Assess the morphology of the erythrocytes.
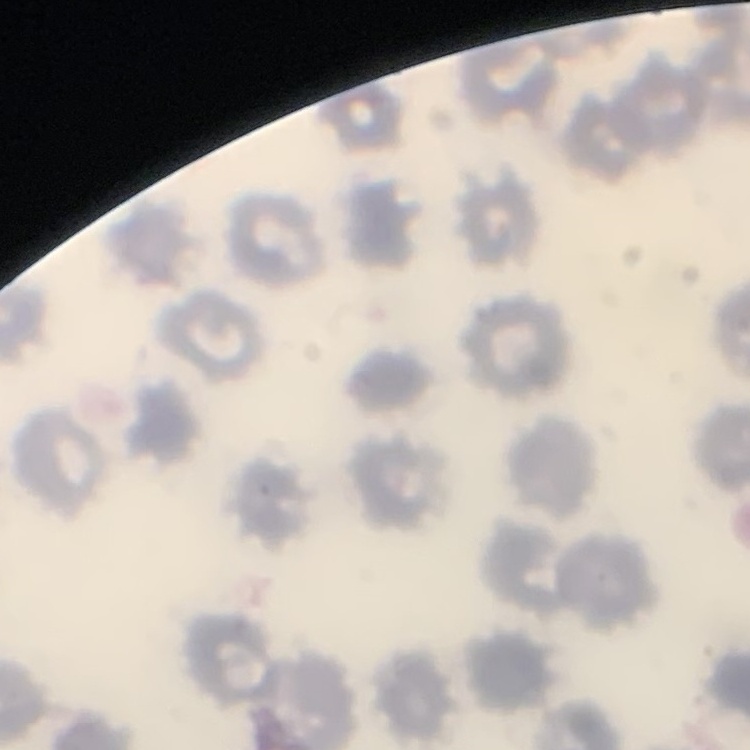
They show no rouleaux formation.

Summary:
  - Image type: square crop of a larger photomicrograph
  - Stain: Field's or Giemsa
  - Preparation: thin blood film